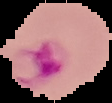

Summary:
  - Malaria status: uninfected
  - Image size: 112×103 pixels
  - Preparation: thin blood smear
  - Image type: segmented cell region on a black background